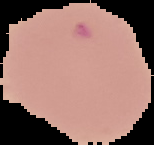

Summary:
  - Image size: 154×145 pixels
  - Malaria status: uninfected
  - Preparation: thin blood film
  - Image type: segmented cell region with the area outside set to black